Locate every blood parasite and identify its species.
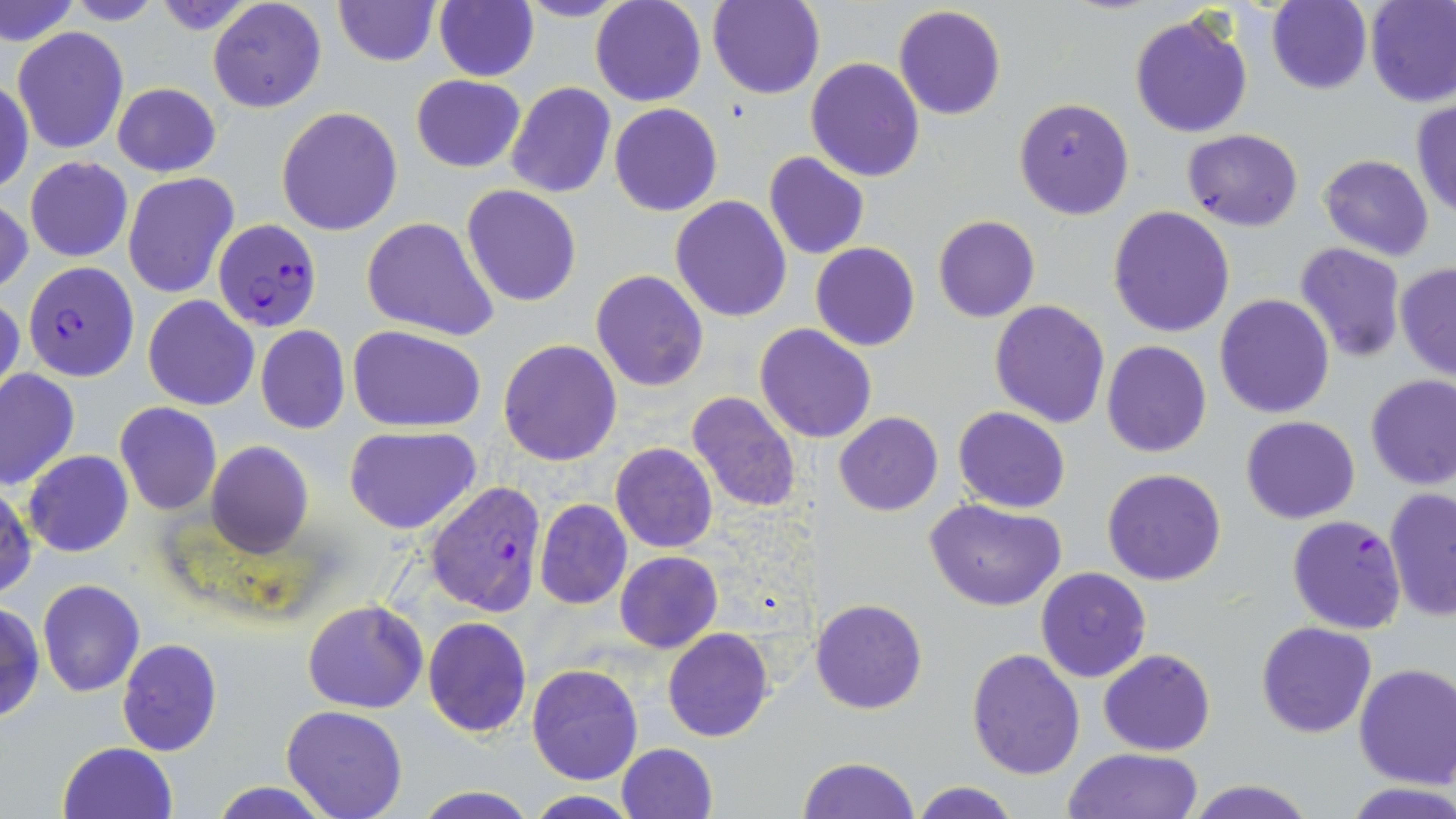
Approximate bounding boxes as (x1, y1, x2, y2) in pixels.
Plasmodium falciparum-infected red blood cells: (213, 218, 322, 331), (21, 261, 140, 382), (425, 481, 549, 615), (1287, 514, 1408, 635).
No Plasmodium ovale, Plasmodium malariae, Plasmodium vivax, Babesia divergens, or Trypanosoma brucei observed.

Uninfected red blood cell locations: (1, 0, 77, 46), (63, 0, 168, 26), (206, 0, 327, 113), (334, 0, 439, 67), (434, 0, 538, 82), (511, 0, 634, 22), (590, 0, 706, 107), (707, 0, 824, 99), (1365, 0, 1456, 108), (1266, 1, 1373, 94), (893, 4, 1006, 120), (1129, 11, 1254, 138), (13, 28, 129, 154), (806, 57, 925, 183), (0, 74, 33, 197), (411, 74, 526, 173), (111, 81, 221, 177), (504, 81, 617, 199), (1015, 97, 1134, 220), (1410, 100, 1456, 220), (609, 103, 723, 216), (276, 106, 403, 235), (1183, 128, 1304, 231), (763, 151, 870, 260), (1318, 153, 1435, 261), (25, 156, 133, 263), (122, 172, 240, 299), (461, 185, 581, 306), (671, 195, 792, 322), (0, 197, 33, 298), (1103, 206, 1231, 338), (933, 215, 1039, 322), (361, 216, 500, 341), (810, 242, 919, 351), (1294, 243, 1407, 363), (1394, 262, 1456, 381), (590, 269, 709, 392), (1213, 293, 1335, 419), (0, 294, 25, 410), (143, 294, 259, 412), (989, 299, 1110, 430), (754, 323, 878, 443), (254, 324, 351, 434), (349, 325, 487, 432), (499, 339, 621, 466), (1100, 339, 1212, 458), (0, 369, 80, 491), (1365, 375, 1456, 490), (684, 390, 801, 514), (114, 402, 222, 515), (953, 406, 1071, 513), (833, 411, 943, 515), (1242, 416, 1361, 523), (343, 425, 482, 533), (206, 441, 312, 558), (610, 443, 718, 553), (24, 450, 134, 558), (1101, 468, 1227, 586), (1, 482, 37, 602), (1383, 489, 1454, 622), (925, 498, 1067, 612), (535, 499, 633, 609), (615, 551, 723, 653), (1035, 566, 1152, 684), (37, 579, 147, 696), (811, 598, 927, 715), (0, 600, 45, 725), (302, 600, 428, 714), (423, 615, 531, 739), (1257, 621, 1376, 737), (663, 628, 774, 743), (116, 639, 222, 756), (967, 648, 1085, 778), (1100, 648, 1216, 755), (527, 662, 643, 786), (1353, 662, 1456, 788), (282, 706, 406, 819), (58, 741, 179, 819), (615, 742, 718, 819), (1060, 747, 1205, 818), (796, 756, 921, 819), (1182, 779, 1315, 819), (208, 780, 337, 818), (908, 780, 1022, 819), (1341, 781, 1456, 818), (411, 786, 539, 819), (521, 791, 643, 818). Slide-level diagnosis: Plasmodium falciparum. Light microscopy. 1000x magnification. Thin blood film. May-Grünwald-Giemsa-stained preparation. One field of a larger specimen. Image is 1456×819 pixels.